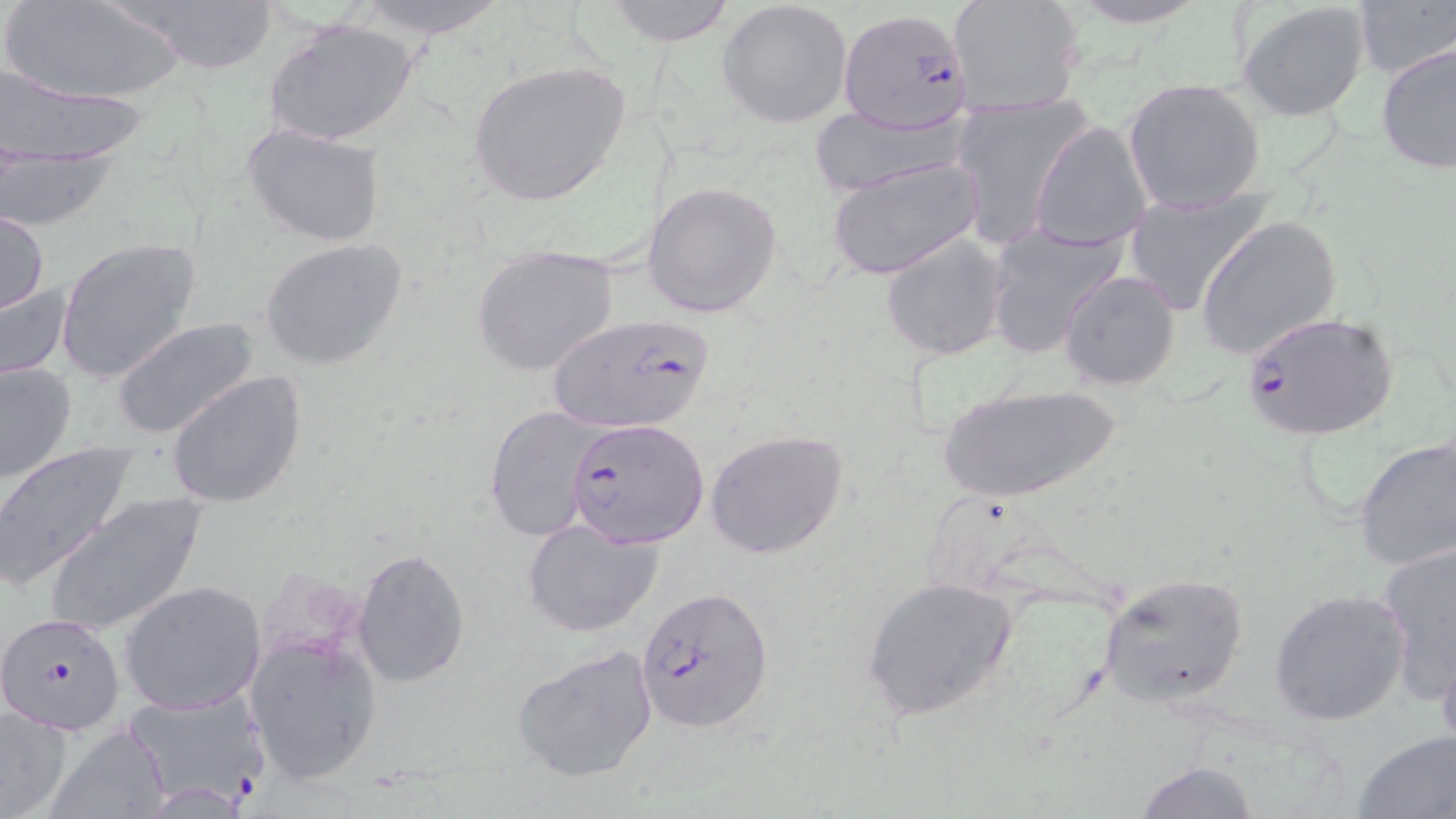

Approximate bounding boxes as (x1, y1, x2, y2) in pixels. Plasmodium falciparum-infected red blood cell locations: (839, 7, 975, 133), (1239, 310, 1395, 442), (547, 313, 718, 433), (567, 417, 709, 550), (636, 586, 775, 731), (1, 613, 127, 733), (123, 687, 268, 809). Uninfected red blood cell locations: (3, 0, 189, 105), (115, 0, 284, 72), (341, 0, 517, 42), (600, 0, 736, 45), (718, 0, 854, 128), (946, 0, 1088, 116), (1054, 0, 1217, 29), (1351, 0, 1456, 81), (1236, 1, 1370, 120), (266, 17, 419, 147), (1374, 41, 1456, 175), (467, 60, 632, 207), (1, 67, 155, 164), (1122, 77, 1266, 215), (946, 91, 1090, 245), (807, 105, 972, 197), (1029, 119, 1154, 252), (242, 124, 388, 247), (2, 154, 117, 233), (827, 157, 983, 280), (642, 181, 785, 318), (1122, 189, 1272, 317), (1, 210, 49, 316), (1197, 216, 1340, 361), (982, 219, 1130, 361), (879, 231, 1008, 360), (55, 236, 203, 384), (261, 238, 410, 372), (471, 245, 619, 379), (1058, 268, 1182, 391), (0, 272, 73, 386), (112, 316, 265, 442), (1, 360, 77, 485), (166, 370, 307, 509), (932, 382, 1124, 505), (484, 404, 605, 542), (704, 428, 850, 560), (1353, 437, 1456, 572), (0, 444, 139, 590), (43, 493, 207, 638), (521, 518, 663, 637), (1377, 542, 1456, 706), (352, 546, 470, 686), (1098, 571, 1250, 708), (861, 576, 1019, 722), (118, 580, 266, 715), (1267, 588, 1410, 726), (246, 633, 381, 786), (511, 643, 661, 784), (1436, 646, 1456, 754), (0, 705, 76, 818), (46, 726, 170, 819), (1351, 730, 1456, 818), (1131, 761, 1264, 818). Slide-level diagnosis: Plasmodium falciparum. Optical microscopy. Thin blood smear. Single field of view. Image is 1456×819 pixels. 1000x magnification. May-Grünwald-Giemsa stain.